Report the malaria status of this cell.
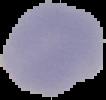
Uninfected.

Summary:
  - Image type: segmented cell region with the area outside set to black
  - Preparation: thin blood smear
  - Image size: 106×100 pixels